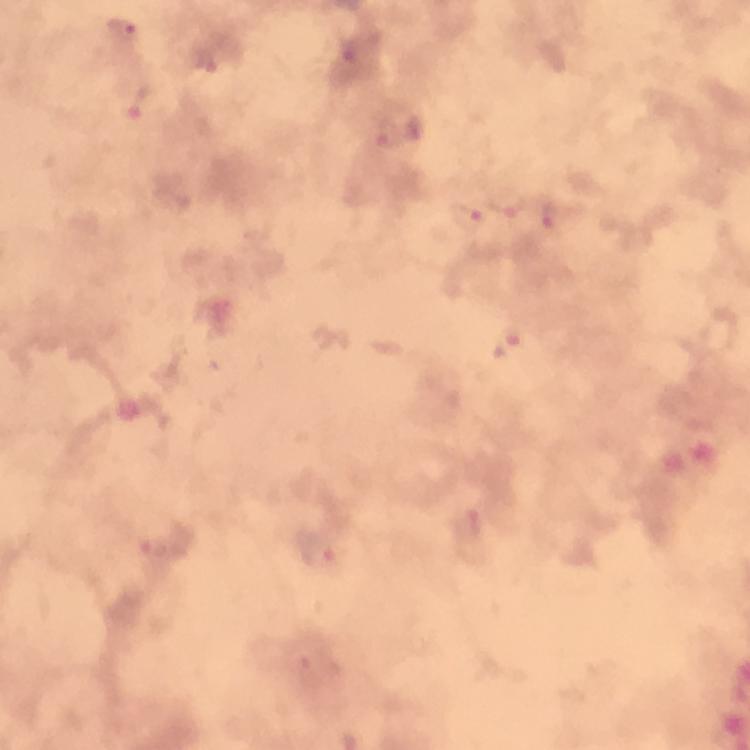
stain = Giemsa
image size = 750×750 pixels
preparation = thick blood film
cropped from = one field of view
immersion oil = used
Plasmodium parasite locations = approximate centers as {x, y} in pixels: {120, 29}, {348, 53}, {204, 61}, {140, 104}, {414, 129}, {385, 133}, {507, 204}, {547, 213}, {467, 217}, {507, 345}, {468, 525}, {156, 547}, {318, 550}, {308, 667}
context = from a diagnostic examination for malaria
capture = smartphone mounted on the microscope
magnification = 100x